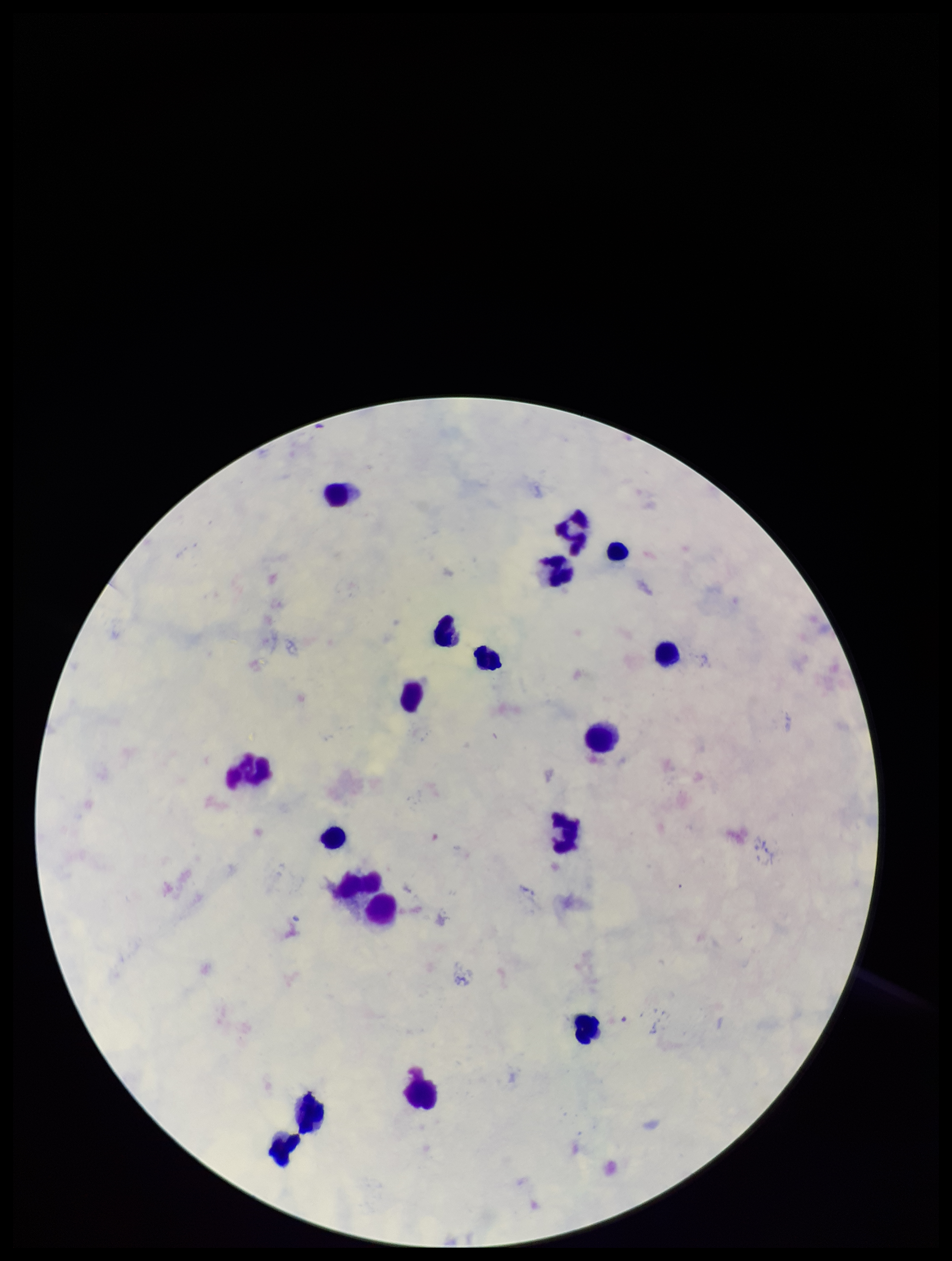
Parasite count: 0. Plasmodium parasites: none detected. Preparation: thick smear. Giemsa stain. Species reported for this patient: Plasmodium falciparum. Image is 952×1261 pixels. Photographed through the microscope eyepiece with a smartphone camera. Patient malaria status: infected. One field from this slide. Leukocyte count: 17.